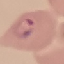
result = malaria parasites identified
capture = smartphone through the microscope eyepiece
stain = Giemsa
preparation = thin blood smear
image type = cell patch, automatically extracted from a larger field of view and resized to 64 × 64 pixels